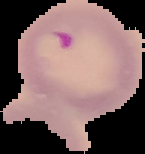

Summary:
  - Image size: 145×154 pixels
  - Malaria status: parasitized
  - Image type: segmented cell region with the area outside set to black
  - Preparation: thin blood film